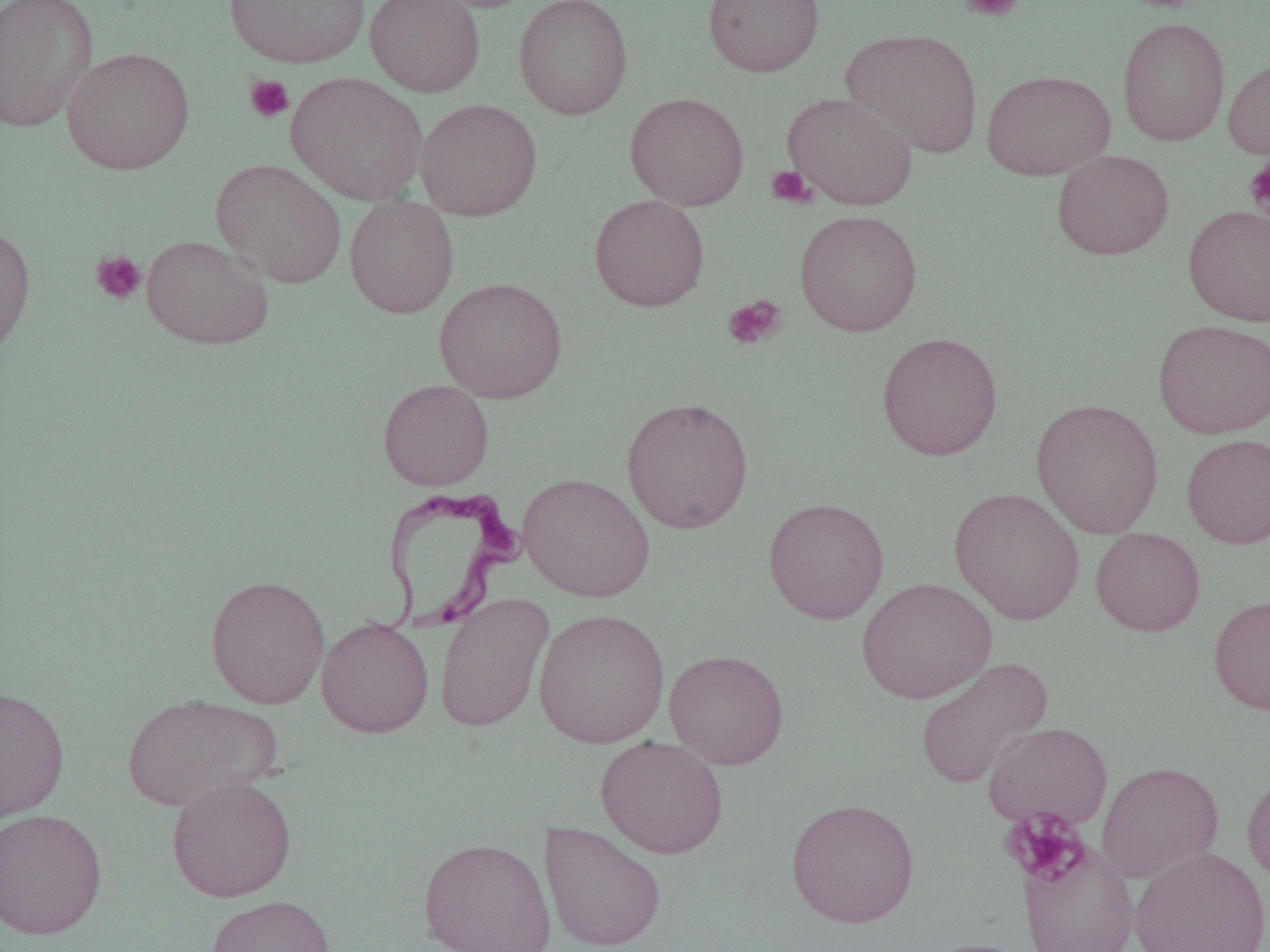

Approximate bounding boxes as [x1, y1, x2, y2] in pixels. Trypanosoma brucei locations: [380, 486, 526, 633]. Platelet locations: [959, 0, 1024, 23], [244, 74, 294, 123], [1244, 157, 1270, 219], [766, 165, 814, 208], [90, 250, 146, 305], [722, 295, 787, 350], [1002, 808, 1090, 887]. Uninfected red blood cell locations: [0, 0, 98, 133], [225, 0, 370, 68], [365, 0, 486, 97], [423, 0, 539, 13], [513, 0, 633, 120], [703, 0, 825, 77], [1118, 17, 1230, 146], [841, 28, 983, 158], [62, 47, 194, 175], [1223, 57, 1270, 160], [982, 69, 1116, 180], [286, 72, 428, 206], [625, 92, 748, 210], [782, 92, 918, 210], [414, 98, 542, 221], [1052, 149, 1174, 260], [211, 158, 347, 288], [590, 194, 709, 311], [344, 196, 459, 318], [1184, 204, 1270, 326], [795, 209, 922, 336], [0, 224, 35, 360], [141, 234, 273, 350], [434, 277, 567, 403], [1153, 319, 1270, 438], [877, 332, 1003, 461], [378, 379, 493, 491], [621, 396, 754, 534], [1031, 398, 1164, 538], [1182, 433, 1270, 549], [518, 472, 655, 603], [949, 487, 1085, 625], [763, 497, 889, 624], [1090, 527, 1205, 636], [205, 574, 330, 709], [856, 577, 997, 704], [434, 593, 554, 732], [1209, 594, 1270, 715], [533, 608, 670, 748], [316, 617, 434, 738], [664, 649, 789, 769], [914, 656, 1053, 790], [0, 685, 70, 824], [121, 694, 281, 812], [983, 722, 1113, 829], [595, 735, 729, 859], [1096, 760, 1225, 883], [1241, 768, 1270, 885], [165, 775, 297, 903], [786, 797, 920, 928], [0, 808, 108, 940], [540, 821, 667, 952], [418, 837, 556, 951], [1018, 839, 1140, 952], [1129, 846, 1270, 952], [205, 894, 335, 952], [916, 937, 1040, 952]. Slide-level diagnosis: Trypanosoma brucei. One field of a larger specimen. Optical microscopy. Image is 1270×952 pixels. 1000x magnification. Thin blood film.